Describe the morphology of the red blood cells.
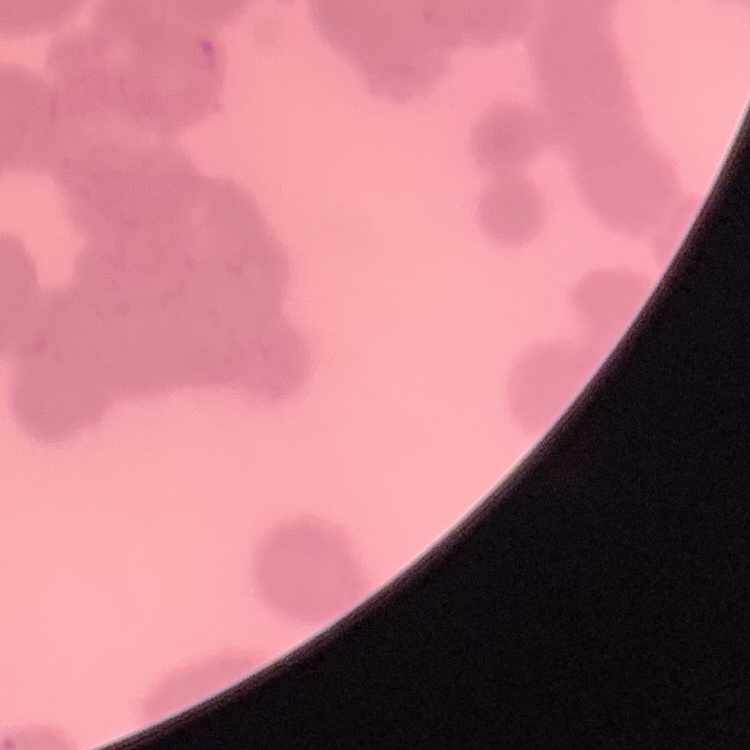

They show rouleaux formation.

Summary:
  - Stain: Field's or Giemsa
  - Image type: one tile cut from a larger photomicrograph
  - Preparation: thin blood smear